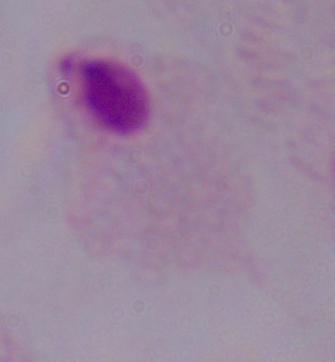
Summary:
  - Modality: micrograph
  - Identification: trichomonad
  - Magnification: 1000x